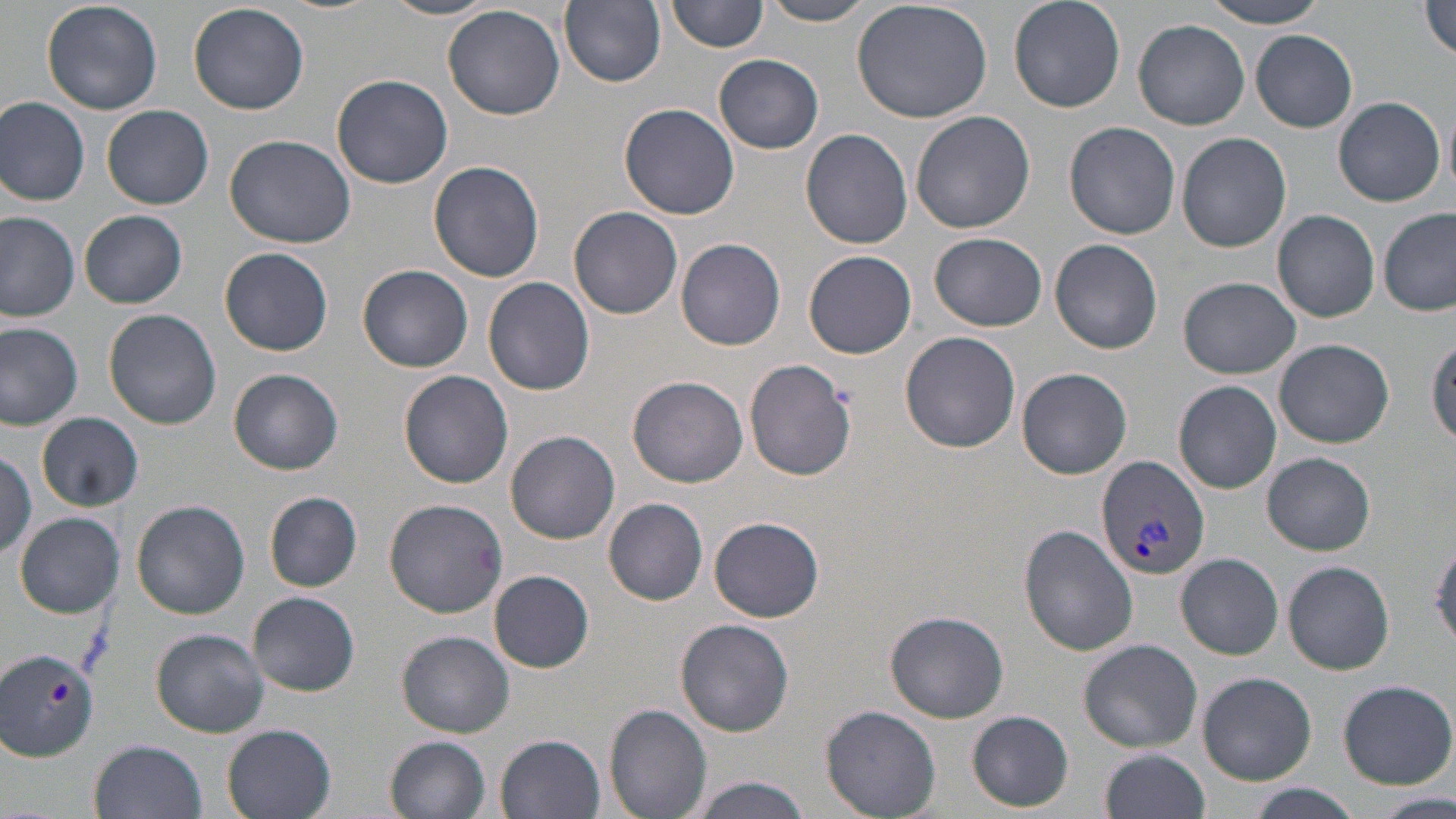

Approximate bounding boxes as [x1, y1, x2, y2] in pixels. Uninfected red blood cell locations: [42, 0, 163, 115], [380, 0, 503, 21], [669, 0, 770, 53], [1008, 0, 1124, 112], [560, 1, 667, 87], [760, 1, 876, 25], [851, 1, 994, 124], [1199, 1, 1335, 27], [188, 2, 311, 115], [1418, 2, 1456, 62], [442, 4, 566, 120], [1134, 18, 1251, 129], [1251, 30, 1358, 132], [714, 54, 824, 155], [332, 73, 455, 189], [0, 96, 90, 205], [1334, 96, 1446, 206], [1442, 97, 1456, 199], [620, 102, 739, 220], [101, 104, 214, 209], [911, 111, 1037, 234], [1064, 121, 1180, 239], [800, 128, 913, 248], [1176, 131, 1291, 252], [224, 134, 357, 248], [429, 161, 544, 283], [569, 205, 683, 319], [1378, 208, 1454, 315], [79, 209, 188, 308], [1273, 210, 1379, 321], [0, 212, 80, 322], [931, 231, 1048, 330], [675, 239, 787, 351], [1049, 239, 1164, 353], [220, 247, 334, 355], [804, 250, 916, 357], [357, 264, 473, 372], [485, 277, 594, 396], [1177, 277, 1301, 379], [103, 309, 222, 429], [0, 322, 83, 429], [899, 331, 1021, 453], [1428, 336, 1456, 443], [1274, 338, 1394, 448], [743, 358, 856, 481], [229, 367, 344, 474], [1016, 367, 1133, 478], [399, 370, 514, 488], [628, 375, 748, 488], [1173, 380, 1282, 493], [38, 412, 143, 511], [505, 429, 621, 544], [0, 450, 37, 559], [1262, 452, 1376, 555], [264, 492, 362, 592], [603, 496, 708, 604], [383, 497, 510, 618], [131, 499, 250, 618], [15, 511, 124, 617], [709, 515, 823, 622], [1020, 524, 1138, 656], [1428, 532, 1456, 652], [1176, 553, 1283, 658], [1280, 560, 1395, 674], [489, 570, 594, 672], [247, 592, 362, 695], [882, 610, 1010, 724], [674, 617, 794, 736], [152, 628, 270, 738], [397, 631, 513, 737], [1078, 638, 1203, 752], [1196, 671, 1318, 786], [1336, 678, 1456, 789], [604, 703, 713, 818], [821, 704, 941, 817], [968, 710, 1073, 811], [221, 724, 338, 819], [495, 733, 606, 818], [384, 735, 491, 819], [88, 739, 208, 819], [1098, 749, 1211, 819], [683, 775, 816, 817], [1370, 791, 1453, 819]. Plasmodium vivax-infected red blood cell locations: [1096, 455, 1210, 581]. Slide-level diagnosis: Plasmodium vivax. Thin blood film. Captured at 1000x magnification. May-Grünwald-Giemsa-stained preparation. Optical microscopy. Image is 1456×819 pixels. Single field of view.